Locate every malaria parasite and every leukocyte.
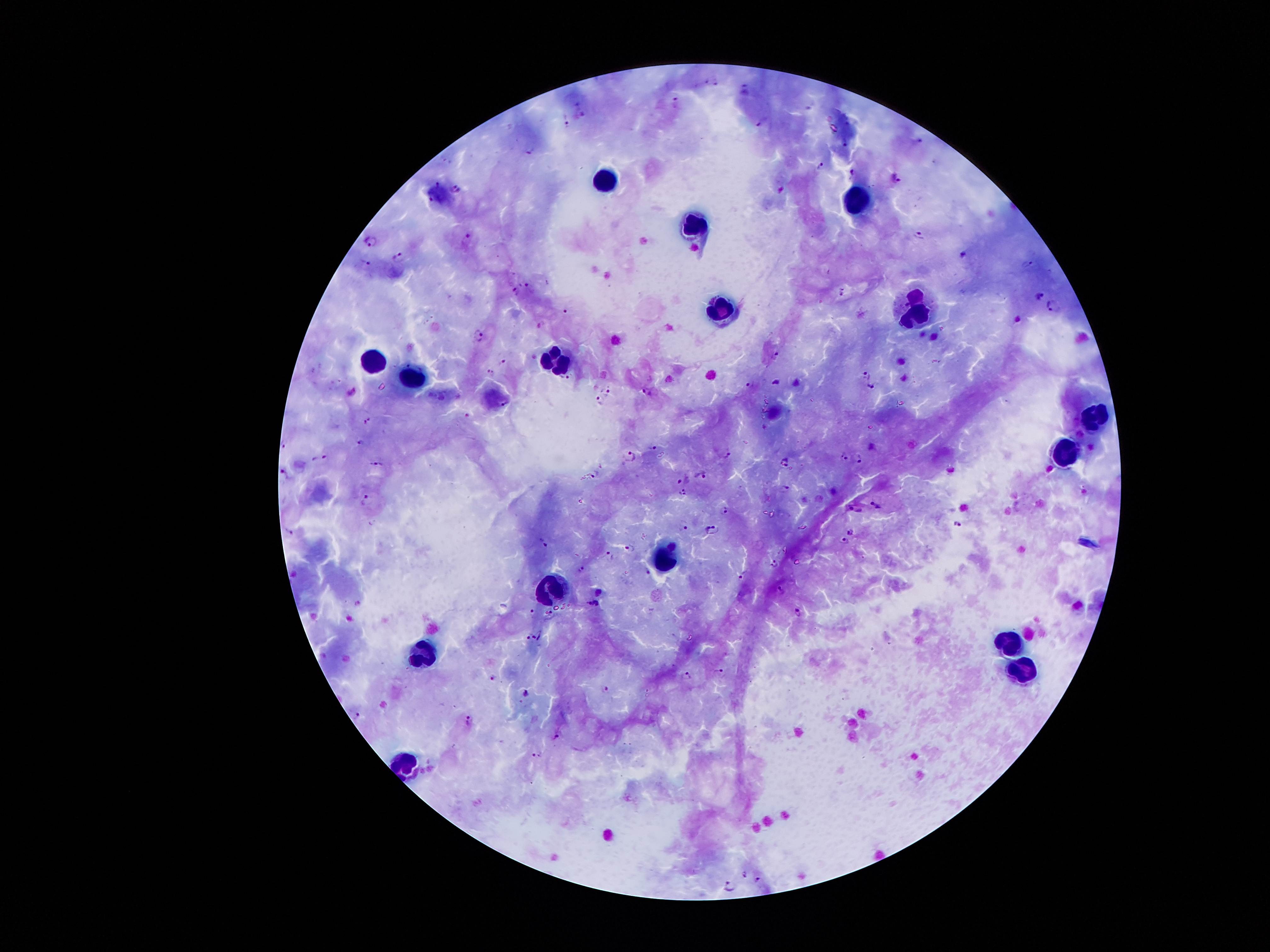

Approximate centers as (x, y) in pixels.
Malaria parasites: (713, 79), (746, 90), (675, 100), (810, 106), (581, 114), (761, 119), (565, 120), (529, 151), (821, 164), (853, 170), (896, 177), (439, 185), (455, 187), (431, 198), (920, 235), (468, 238), (373, 239), (964, 253), (399, 255), (366, 261), (1029, 262), (529, 287), (515, 289), (841, 290), (1039, 294), (1050, 305), (564, 310), (479, 333), (775, 355), (503, 359), (491, 370), (868, 372), (565, 378), (749, 381), (775, 381), (870, 384), (608, 389), (647, 389), (599, 397), (503, 404), (368, 420), (360, 443), (284, 445), (654, 447), (726, 453), (633, 454), (861, 456), (320, 457), (845, 457), (784, 462), (377, 463), (284, 472), (595, 473), (701, 475), (681, 480), (786, 486), (683, 490), (364, 499), (879, 507), (724, 508), (855, 509), (958, 524), (685, 527), (712, 529), (849, 530), (288, 531), (843, 541), (544, 543), (630, 548), (608, 555), (774, 562), (582, 568), (648, 572), (743, 574), (780, 591), (595, 604), (531, 611), (796, 612), (550, 614), (540, 632), (534, 637), (527, 638), (720, 670), (688, 675), (491, 676), (606, 689), (526, 692), (356, 713), (470, 719), (555, 735), (535, 754), (744, 872), (757, 878), (729, 885).
Leukocytes: (600, 183), (857, 195), (695, 218), (720, 306), (917, 314), (553, 362), (370, 363), (415, 376), (1098, 413), (1065, 450), (664, 556), (553, 589), (1007, 642), (423, 655), (1027, 673), (401, 764).

Image is 1270×952 pixels. One field from this slide. 100x magnification. Smartphone photograph taken through the microscope eyepiece. Patient malaria status: infected with Plasmodium falciparum. Thick blood film. Giemsa stain.